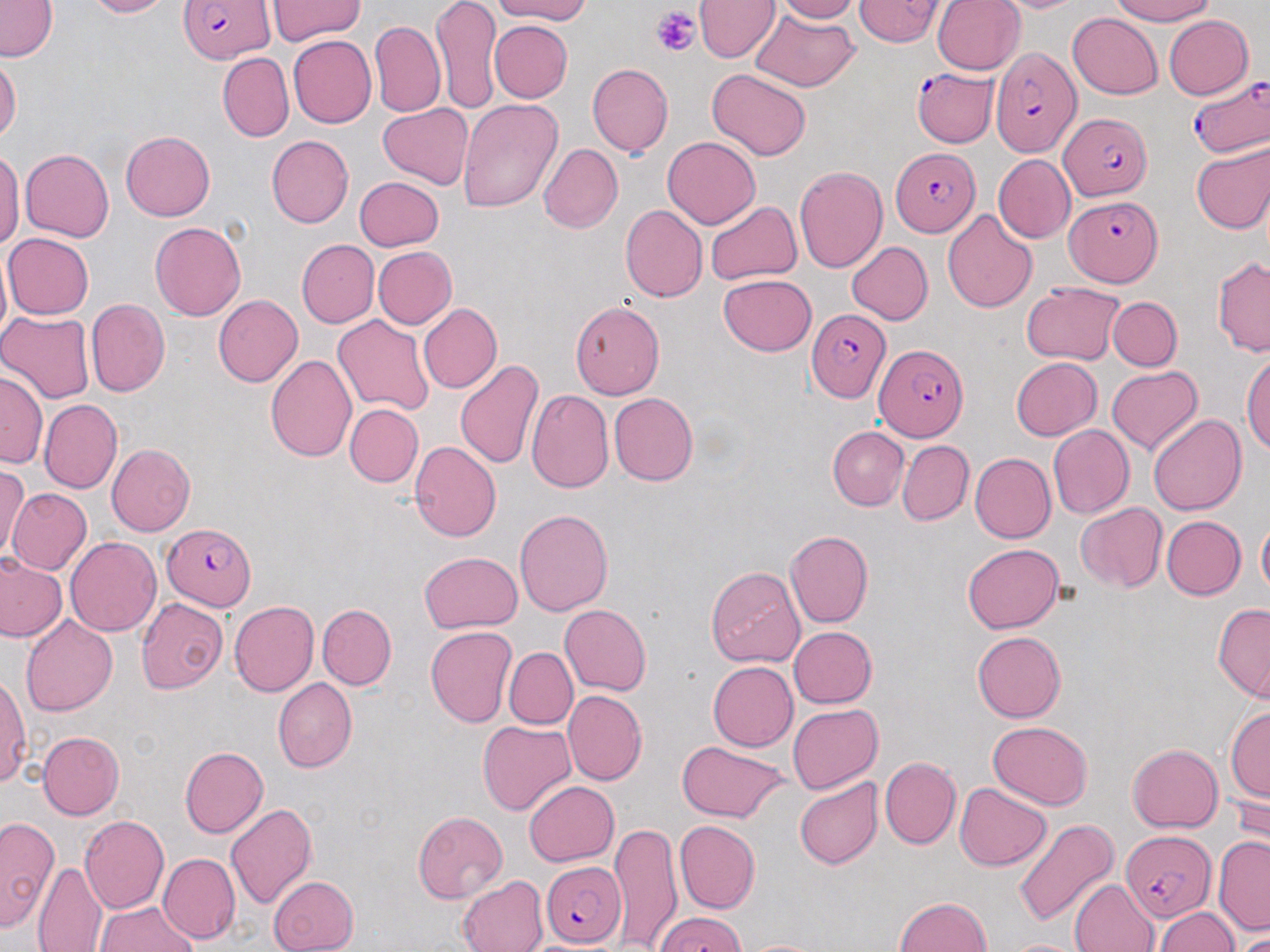
{
  "slide_level_diagnosis": "Plasmodium falciparum",
  "platelet_locations": "approximate bounding boxes as [x1, y1, x2, y2] in pixels: [651, 5, 699, 57]",
  "image_size": "1270×952 pixels",
  "uninfected_red_blood_cell_locations": "approximate bounding boxes as [x1, y1, x2, y2] in pixels: [83, 0, 175, 18], [432, 0, 500, 114], [491, 0, 593, 24], [694, 0, 779, 61], [773, 0, 861, 23], [855, 0, 945, 46], [931, 0, 1026, 75], [988, 0, 1092, 13], [1111, 0, 1217, 25], [0, 1, 58, 62], [266, 1, 366, 43], [762, 4, 860, 43], [749, 8, 858, 91], [1068, 12, 1162, 100], [1164, 15, 1254, 99], [370, 20, 445, 117], [488, 20, 572, 102], [288, 35, 377, 128], [218, 52, 293, 141], [0, 55, 21, 142], [587, 63, 673, 157], [706, 69, 811, 161], [456, 98, 564, 213], [377, 103, 473, 191], [121, 130, 214, 220], [266, 135, 354, 228], [663, 136, 760, 229], [1190, 140, 1270, 234], [538, 143, 622, 233], [20, 148, 114, 242], [0, 150, 23, 249], [993, 155, 1076, 243], [794, 167, 887, 272], [353, 177, 445, 252], [706, 201, 801, 285], [620, 204, 707, 302], [942, 209, 1038, 312], [150, 222, 245, 321], [3, 233, 94, 319], [297, 240, 379, 327], [847, 241, 933, 324], [0, 245, 11, 350], [373, 246, 457, 328], [1212, 256, 1270, 356], [718, 274, 816, 355], [1020, 281, 1126, 365], [213, 296, 302, 387], [1108, 296, 1181, 371], [85, 299, 170, 398], [570, 301, 664, 398], [419, 304, 503, 394], [0, 311, 95, 403], [332, 315, 433, 416], [1242, 352, 1270, 454], [265, 355, 356, 462], [1011, 357, 1102, 439], [454, 360, 546, 471], [1106, 366, 1202, 455], [0, 370, 47, 468], [526, 389, 614, 493], [609, 393, 699, 486], [40, 399, 122, 493], [345, 404, 423, 487], [1148, 414, 1247, 516], [1048, 424, 1134, 519], [828, 427, 909, 511], [897, 440, 973, 525], [409, 441, 501, 541], [106, 443, 196, 537], [970, 453, 1055, 543], [1, 466, 28, 562], [7, 487, 92, 575], [1075, 502, 1166, 591], [515, 508, 613, 616], [1162, 516, 1246, 601], [1257, 517, 1270, 598], [785, 530, 873, 628], [65, 536, 161, 637], [962, 544, 1064, 632], [418, 551, 523, 633], [0, 554, 66, 642], [705, 565, 806, 667], [57, 568, 152, 682], [136, 598, 229, 694], [229, 600, 319, 696], [1213, 603, 1270, 702], [317, 604, 396, 690], [560, 605, 651, 696], [20, 614, 118, 716], [425, 625, 518, 727], [788, 626, 876, 709], [972, 631, 1066, 723], [505, 647, 578, 729], [707, 661, 797, 751], [0, 673, 31, 788], [273, 678, 356, 772], [564, 690, 647, 786], [788, 704, 883, 793], [1227, 705, 1270, 802], [478, 720, 576, 815], [989, 721, 1093, 809], [39, 730, 125, 819], [676, 741, 793, 824], [1127, 744, 1223, 832], [179, 747, 269, 838], [879, 756, 960, 850], [794, 777, 883, 870], [1231, 779, 1270, 861], [524, 781, 619, 865], [955, 782, 1051, 870], [226, 804, 317, 909], [413, 811, 507, 903], [78, 815, 169, 914], [0, 816, 58, 931], [1013, 819, 1119, 928], [674, 820, 761, 914], [609, 821, 683, 951], [1214, 835, 1270, 935], [157, 852, 240, 944], [32, 862, 107, 952], [267, 875, 359, 952], [456, 875, 548, 952], [1070, 878, 1160, 951], [894, 896, 992, 951], [95, 902, 199, 952], [1154, 907, 1239, 951], [1236, 930, 1270, 952], [736, 938, 835, 952], [1003, 939, 1088, 952]",
  "plasmodium_falciparum_infected_red_blood_cell_locations": "approximate bounding boxes as [x1, y1, x2, y2] in pixels: [178, 0, 274, 65], [990, 47, 1079, 157], [912, 61, 999, 149], [1187, 76, 1268, 158], [1058, 112, 1152, 199], [892, 147, 978, 236], [1065, 194, 1164, 286], [807, 309, 891, 402], [874, 344, 968, 442], [162, 522, 256, 611], [1120, 830, 1215, 925], [541, 861, 626, 947], [656, 912, 747, 952]",
  "field_of_view": "single",
  "stain": "May-Grünwald-Giemsa",
  "modality": "light microscopy",
  "magnification": "1000x",
  "preparation": "thin blood smear"
}